State which cell type is depicted.
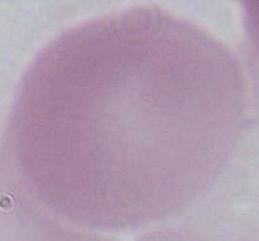
An erythrocyte.

Summary:
  - Magnification: 1000x
  - Modality: micrograph